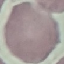 Result: negative for malaria parasites. Photographed with a smartphone camera at the microscope eyepiece. Cell patch, automatically extracted from a larger field of view and resized to 64 × 64 pixels. Giemsa stain. Thin blood film.